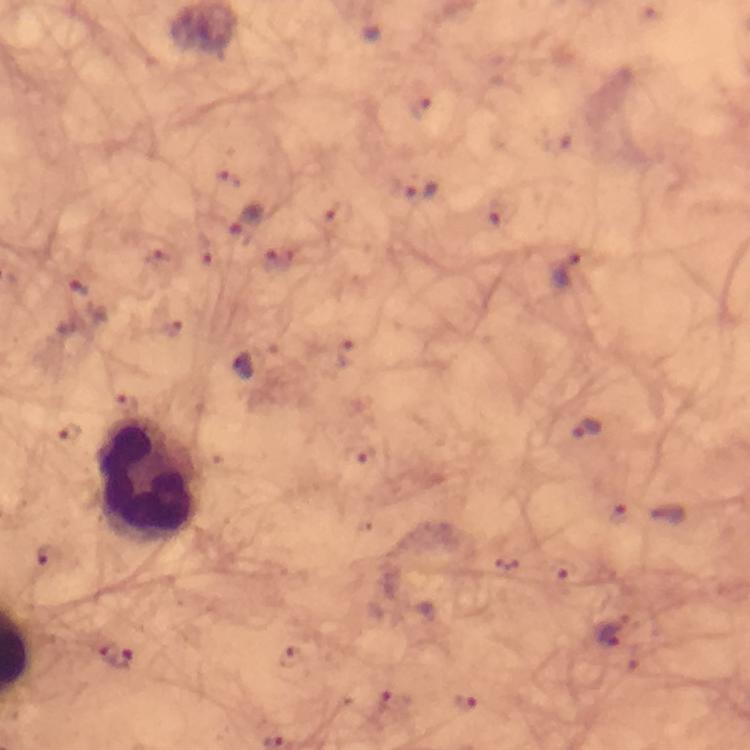
Approximate centers as {x, y} in pixels.
Summary:
  - Leukocyte locations: {150, 480}
  - Malaria parasite locations: {421, 192}, {246, 222}, {569, 269}, {79, 287}, {244, 366}, {588, 430}, {612, 632}, {116, 655}
  - Stain: Giemsa
  - Immersion oil: used
  - Preparation: thick blood smear
  - Magnification: 100x
  - Image size: 750×750 pixels
  - Capture: smartphone mounted on the microscope
  - Context: from a diagnostic examination for malaria
  - Cropped from: one field of view